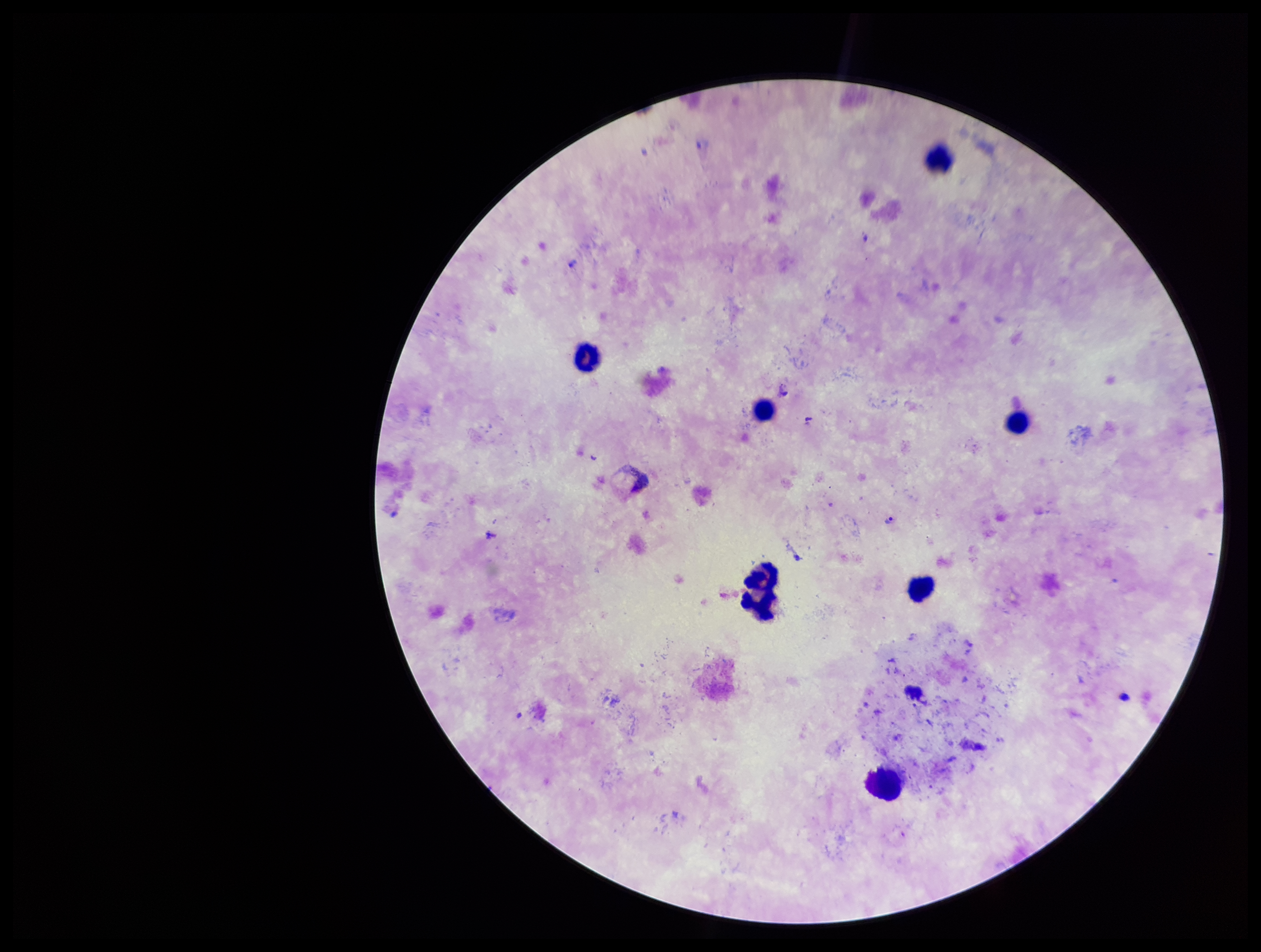
Plasmodium parasites: identified. Patient malaria status: positive. One field from this slide. Species reported for this patient: Plasmodium vivax. Leukocyte count: 8. Image is 1261×952 pixels. Preparation: thick blood smear. Giemsa stain. Parasite count: 1. Photographed through the microscope eyepiece with a smartphone camera.